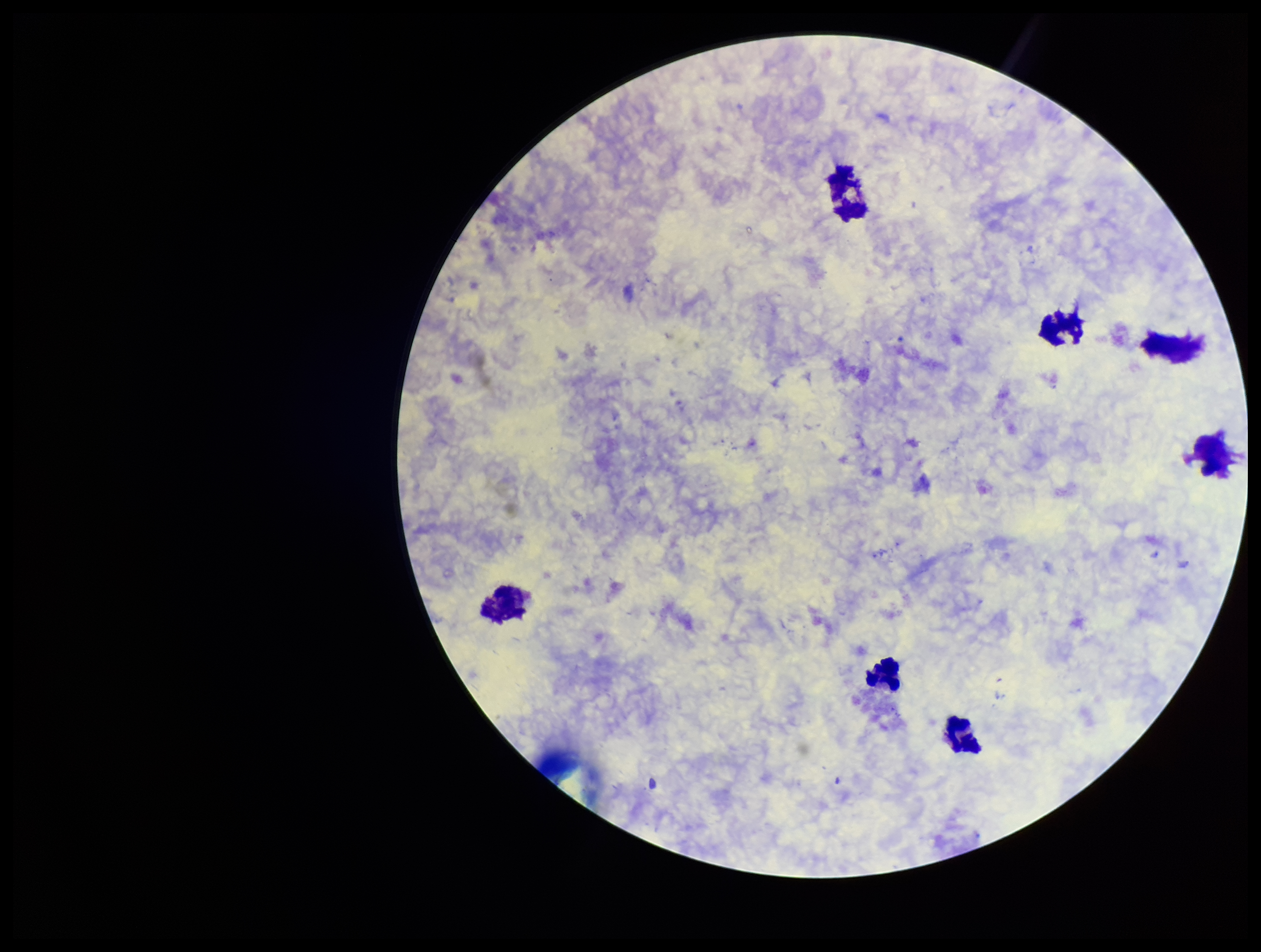
Summary:
  - Patient malaria status: negative
  - Preparation: thick blood smear
  - Field of view: single
  - Leukocyte count: 6
  - Capture: smartphone photograph through the microscope eyepiece
  - Stain: Giemsa
  - Plasmodium parasites: none identified
  - Parasite count: 0
  - Image size: 1261×952 pixels